Report the malaria status of this cell.
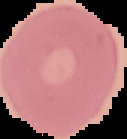
Uninfected.

From a thin blood smear. The area outside the segmented cell region is set to black. Image is 127×139 pixels.